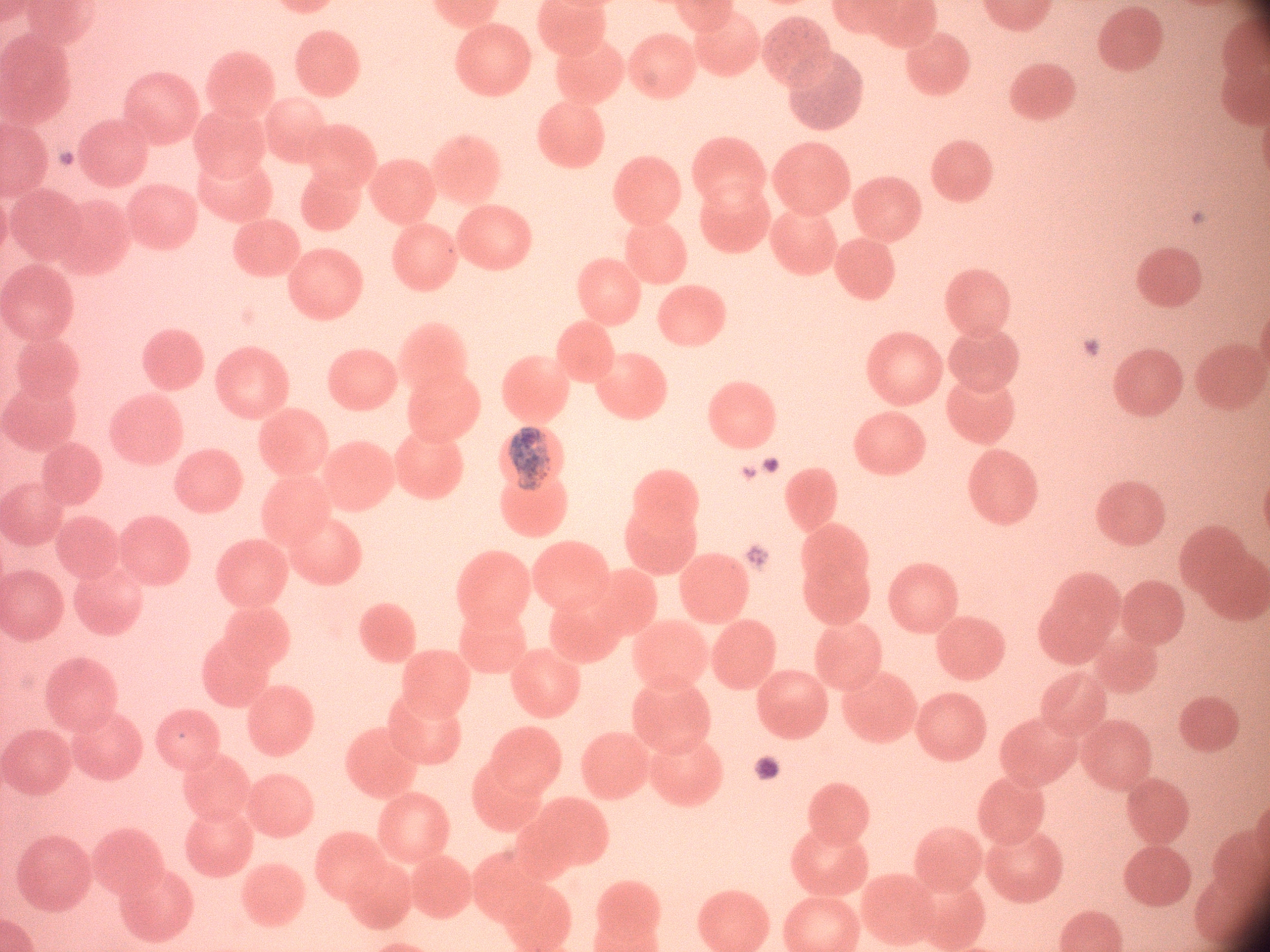

{
  "trophozoite_locations": "approximate bounding boxes as [x1, y1, x2, y2] in pixels, from the source annotation, which is not necessarily exhaustive: [509, 427, 551, 491]",
  "magnification": "100x",
  "microscope": "Leica DM2000 with built-in camera",
  "species": "Plasmodium malariae",
  "field_of_view": "one from this slide",
  "stain": "Giemsa",
  "preparation": "thin blood smear",
  "image_size": "1270×952 pixels"
}